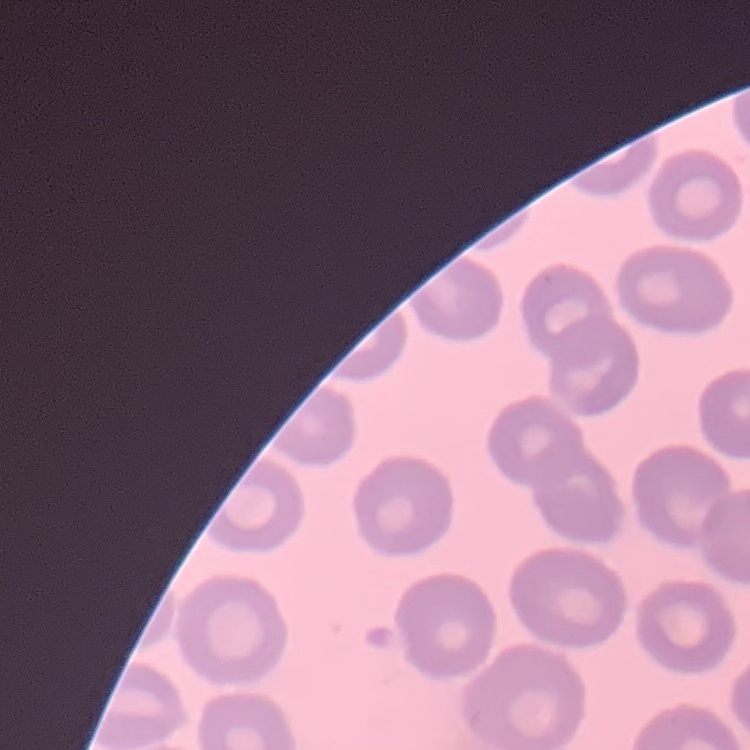 The red blood cells show no rouleaux formation. Field's or Giemsa stain. Square crop of a larger photomicrograph. Thin blood film.